Assess this cell for malaria.
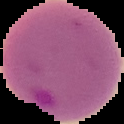

Parasitized.

preparation = thin blood film
image size = 124×124 pixels
image type = cell region segmented out of the field of view; surrounding area masked to black